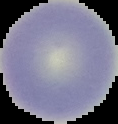
image size = 118×124 pixels
image type = segmented cell region with the area outside set to black
preparation = thin blood smear
malaria status = uninfected